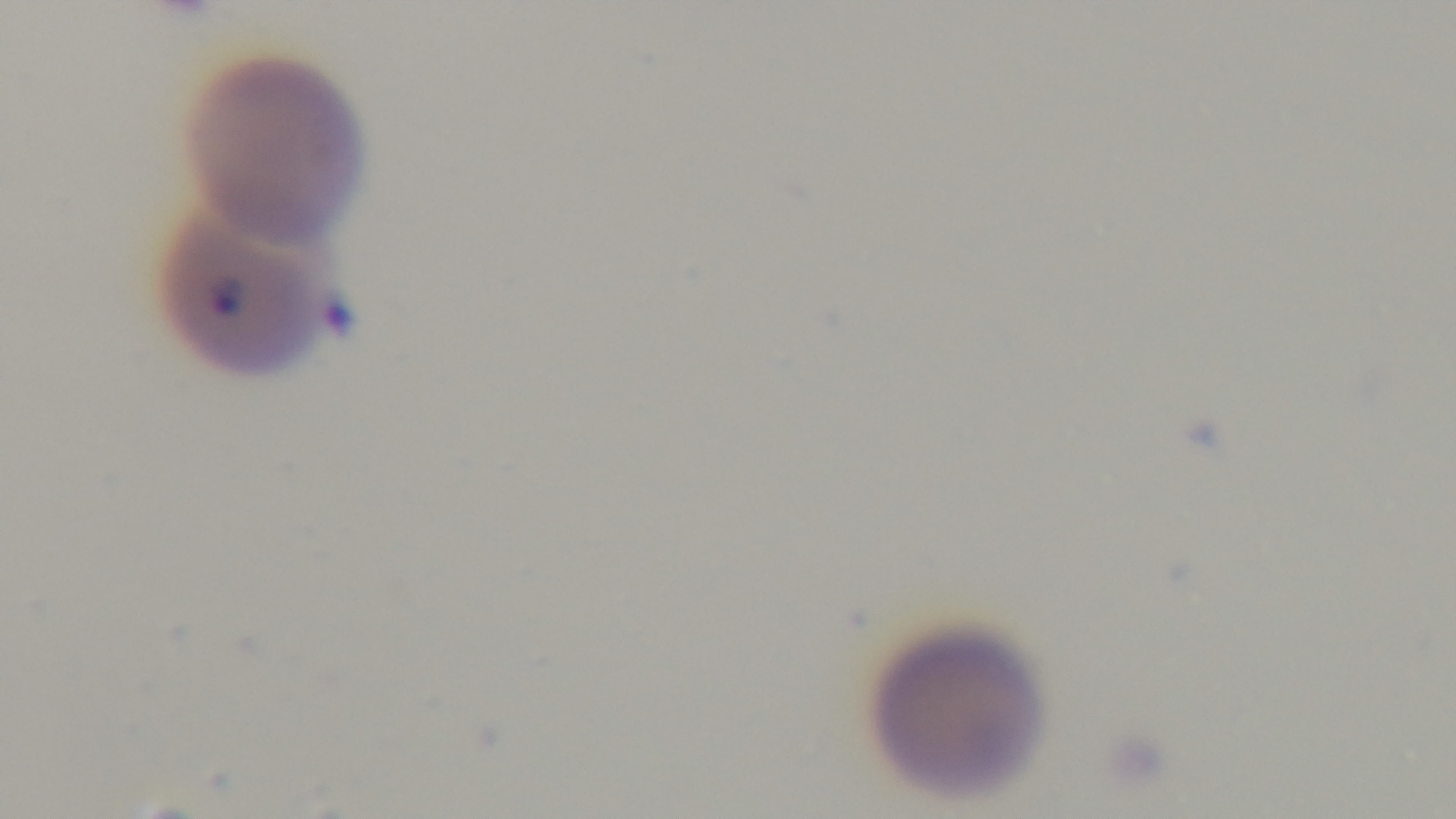

objective = 100x oil immersion
malaria status = infected
preparation = thin
stain = Giemsa
field of view = single
capture = mounted 4K digital camera
modality = light microscopy